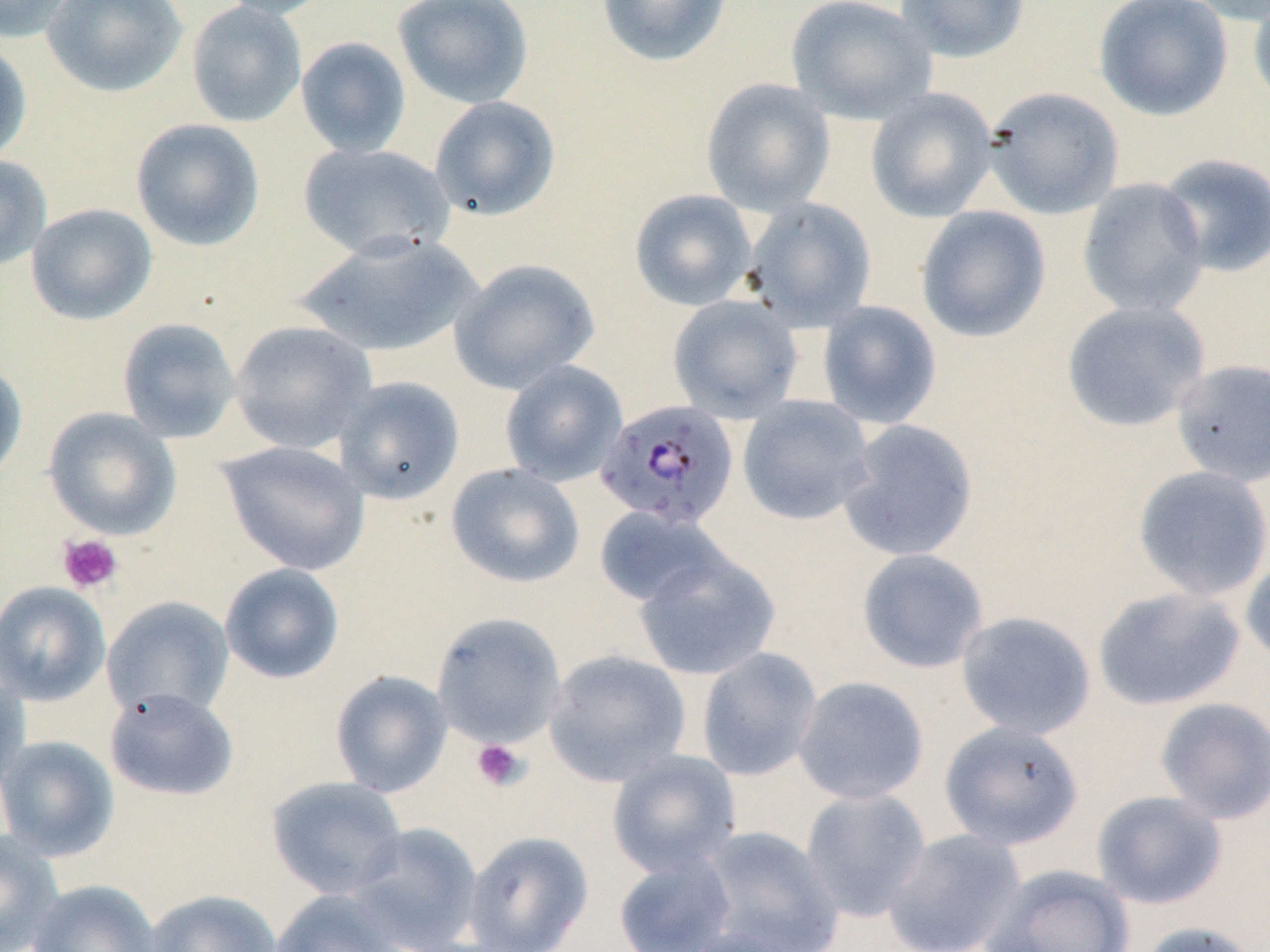

Approximate bounding boxes as named x1/y1/x2/y2 corners in pixels. Uninfected red blood cell locations: (x1=0, y1=0, x2=75, y2=42), (x1=41, y1=0, x2=188, y2=98), (x1=214, y1=0, x2=341, y2=21), (x1=393, y1=0, x2=535, y2=109), (x1=595, y1=0, x2=732, y2=67), (x1=785, y1=0, x2=937, y2=125), (x1=895, y1=0, x2=1030, y2=63), (x1=1094, y1=0, x2=1233, y2=121), (x1=1177, y1=0, x2=1270, y2=26), (x1=1248, y1=0, x2=1270, y2=110), (x1=185, y1=1, x2=307, y2=128), (x1=295, y1=37, x2=411, y2=158), (x1=0, y1=39, x2=32, y2=163), (x1=700, y1=78, x2=836, y2=216), (x1=865, y1=87, x2=998, y2=223), (x1=984, y1=87, x2=1124, y2=219), (x1=429, y1=96, x2=561, y2=221), (x1=130, y1=118, x2=265, y2=251), (x1=298, y1=142, x2=456, y2=260), (x1=1156, y1=153, x2=1270, y2=277), (x1=0, y1=154, x2=52, y2=272), (x1=1077, y1=177, x2=1210, y2=319), (x1=630, y1=189, x2=757, y2=310), (x1=743, y1=197, x2=876, y2=331), (x1=26, y1=203, x2=157, y2=325), (x1=915, y1=206, x2=1051, y2=343), (x1=295, y1=232, x2=482, y2=358), (x1=449, y1=257, x2=600, y2=394), (x1=667, y1=294, x2=804, y2=423), (x1=817, y1=300, x2=942, y2=429), (x1=1060, y1=300, x2=1210, y2=432), (x1=117, y1=317, x2=242, y2=444), (x1=229, y1=320, x2=376, y2=454), (x1=0, y1=359, x2=28, y2=486), (x1=1171, y1=359, x2=1270, y2=487), (x1=499, y1=360, x2=628, y2=487), (x1=333, y1=376, x2=464, y2=505), (x1=737, y1=395, x2=875, y2=526), (x1=43, y1=407, x2=182, y2=540), (x1=837, y1=418, x2=979, y2=562), (x1=216, y1=441, x2=371, y2=576), (x1=445, y1=462, x2=585, y2=589), (x1=1131, y1=465, x2=1270, y2=602), (x1=594, y1=505, x2=730, y2=609), (x1=633, y1=547, x2=781, y2=681), (x1=856, y1=548, x2=989, y2=674), (x1=1240, y1=554, x2=1270, y2=668), (x1=219, y1=563, x2=345, y2=684), (x1=0, y1=581, x2=110, y2=706), (x1=1092, y1=586, x2=1246, y2=711), (x1=102, y1=596, x2=234, y2=719), (x1=955, y1=611, x2=1096, y2=740), (x1=431, y1=612, x2=566, y2=748), (x1=696, y1=647, x2=823, y2=781), (x1=543, y1=649, x2=691, y2=787), (x1=0, y1=667, x2=30, y2=790), (x1=330, y1=669, x2=453, y2=797), (x1=792, y1=676, x2=929, y2=805), (x1=105, y1=687, x2=239, y2=801), (x1=1153, y1=697, x2=1270, y2=823), (x1=939, y1=720, x2=1083, y2=849), (x1=0, y1=735, x2=119, y2=861), (x1=606, y1=749, x2=741, y2=877), (x1=265, y1=776, x2=408, y2=899), (x1=800, y1=787, x2=932, y2=922), (x1=1091, y1=791, x2=1228, y2=910), (x1=347, y1=822, x2=483, y2=951), (x1=697, y1=825, x2=843, y2=952), (x1=881, y1=828, x2=1026, y2=952), (x1=0, y1=829, x2=63, y2=952), (x1=462, y1=830, x2=594, y2=952), (x1=612, y1=852, x2=737, y2=952), (x1=981, y1=864, x2=1135, y2=952), (x1=27, y1=879, x2=162, y2=952), (x1=269, y1=888, x2=408, y2=952), (x1=145, y1=890, x2=283, y2=952), (x1=1135, y1=921, x2=1262, y2=952), (x1=671, y1=927, x2=807, y2=952). Plasmodium falciparum-infected red blood cell locations: (x1=596, y1=400, x2=739, y2=529). Platelet locations: (x1=57, y1=533, x2=123, y2=594), (x1=471, y1=738, x2=529, y2=791). Slide-level diagnosis: Plasmodium falciparum. One field of a larger specimen. Image is 1270×952 pixels. 1000x magnification. May-Grünwald-Giemsa-stained preparation. Light microscopy. Thin blood film.